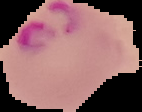
Summary:
  - Preparation: thin blood smear
  - Malaria status: parasitized
  - Image size: 142×112 pixels
  - Image type: segmented cell region with the area outside set to black